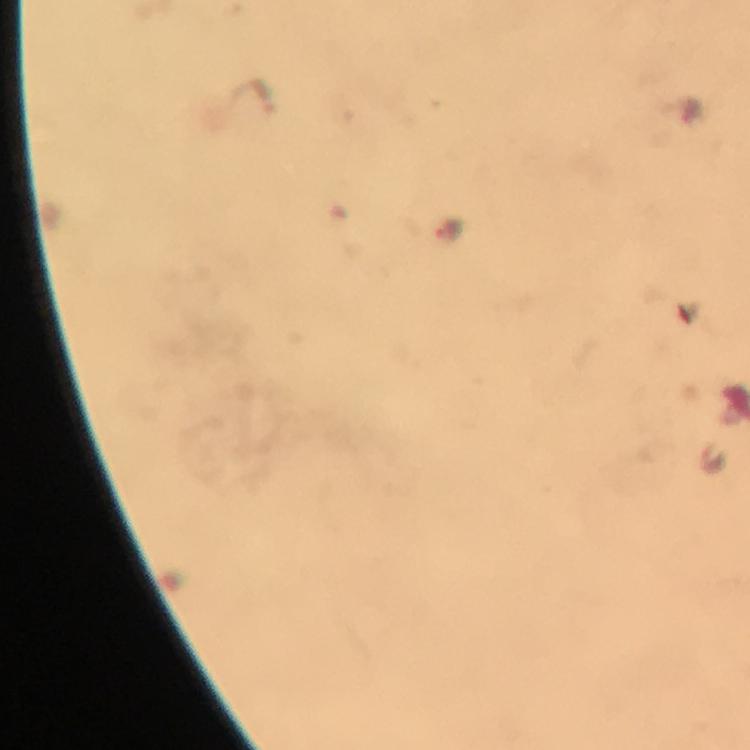
Approximate object centers, in pixels from the top-left corner.
Summary:
  - Plasmodium parasite locations: (x=449, y=227), (x=714, y=459)
  - Magnification: 100x
  - Image size: 750×750 pixels
  - Immersion oil: used
  - Context: from a diagnostic examination for malaria
  - Cropped from: a single field of view
  - Preparation: thick blood smear
  - Stain: Giemsa
  - Capture: smartphone camera through the microscope